Report the malaria status of this cell.
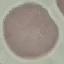

Uninfected.

image type = automatically extracted cell patch, resized to 64 × 64 pixels
capture = smartphone through the microscope eyepiece
preparation = thin blood smear
stain = Giemsa